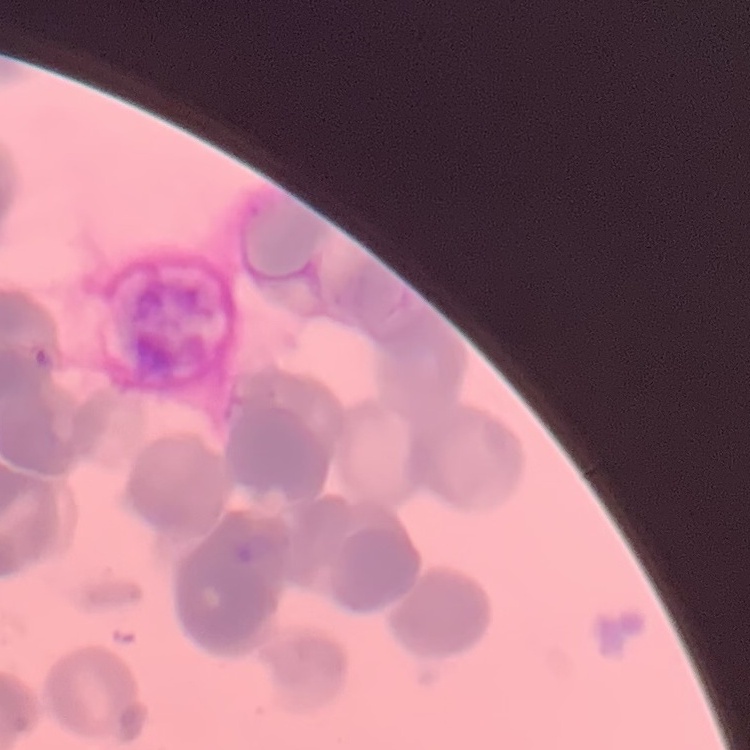

erythrocyte_morphology: rouleaux formation
preparation: thin blood smear
image_type: one tile cut from a larger photomicrograph
stain: Field's or Giemsa